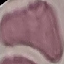

Summary:
  - Result: no malaria parasites seen
  - Stain: Giemsa
  - Preparation: thin blood smear
  - Capture: smartphone through the microscope eyepiece
  - Image type: automatically extracted cell patch, resized to 64 × 64 pixels